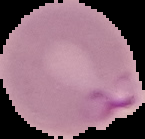
Malaria status: parasitized. From a thin blood film. Image is 145×139 pixels. Cell region segmented out of the field of view; the surrounding area is masked to black.